Report the malaria status of this cell.
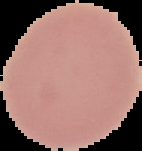
Uninfected.

From a thin blood film. The area outside the segmented cell region is set to black. Image is 142×151 pixels.